Assess this cell for malaria.
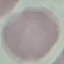

It is uninfected.

{
  "image_type": "cell patch, automatically extracted from a larger field of view and resized to 64 × 64 pixels",
  "stain": "Giemsa",
  "capture": "smartphone through the microscope eyepiece",
  "preparation": "thin smear"
}